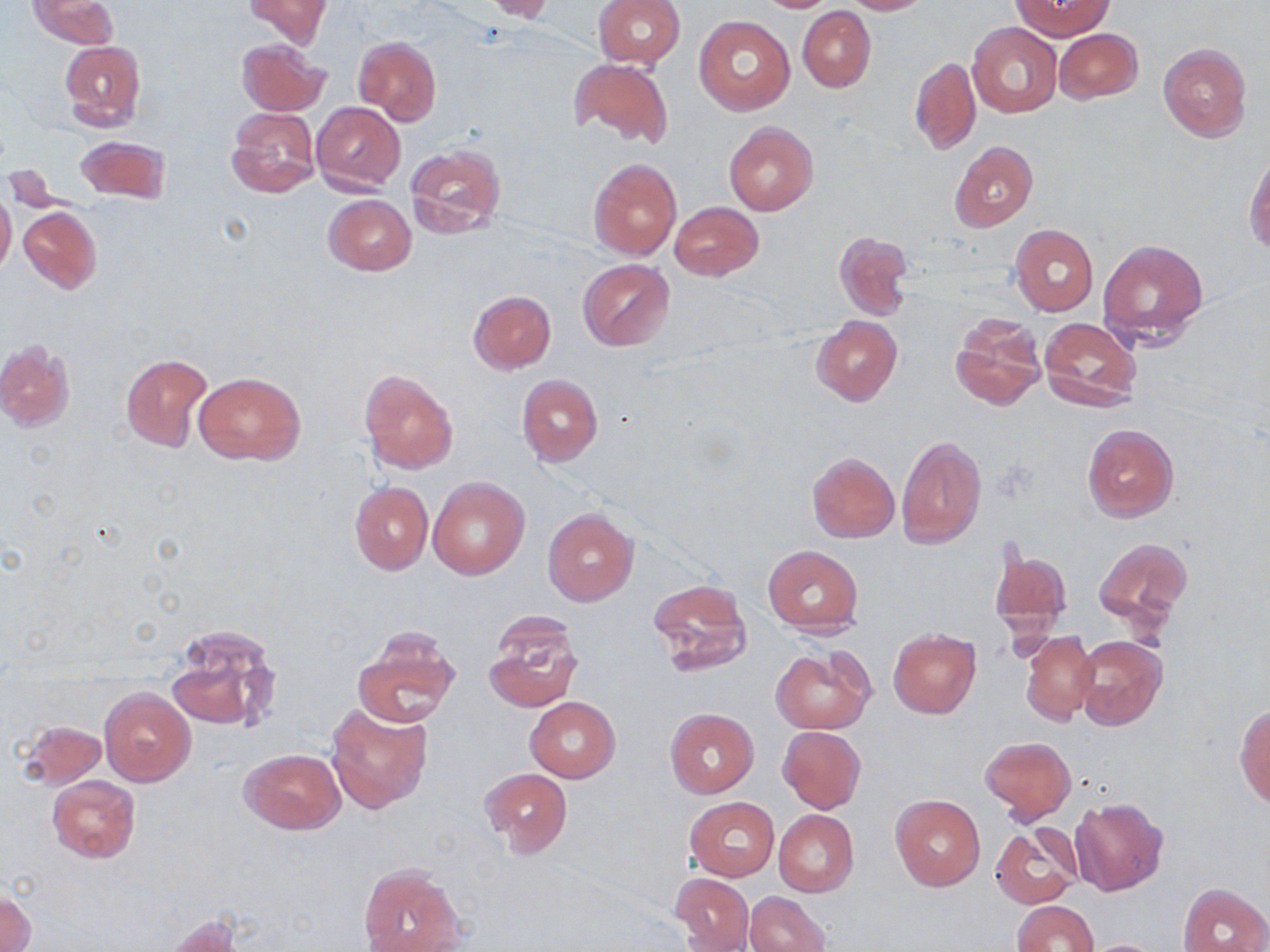

slide-level diagnosis = no evidence of blood parasites
modality = optical microscopy
preparation = thin blood film
image size = 1270×952 pixels
magnification = 1000x
stain = May-Grünwald-Giemsa
field of view = one of a larger specimen
uninfected red blood cell locations = approximate bounding boxes as [x1, y1, x2, y2] in pixels: [27, 0, 119, 50], [243, 0, 330, 49], [483, 0, 558, 23], [594, 0, 684, 69], [753, 0, 839, 13], [841, 0, 932, 14], [1012, 2, 1110, 38], [797, 6, 875, 93], [694, 14, 794, 114], [968, 22, 1061, 118], [1053, 28, 1143, 103], [355, 36, 441, 124], [237, 39, 329, 116], [59, 40, 145, 132], [1157, 43, 1253, 143], [910, 55, 982, 157], [569, 57, 674, 150], [312, 102, 405, 195], [226, 106, 320, 200], [723, 120, 819, 215], [75, 135, 170, 205], [949, 142, 1037, 231], [404, 143, 507, 237], [1245, 149, 1270, 254], [589, 158, 681, 259], [0, 190, 16, 279], [323, 194, 416, 275], [669, 201, 763, 280], [18, 206, 103, 294], [1010, 224, 1097, 316], [832, 230, 915, 322], [1097, 239, 1208, 348], [578, 259, 676, 351], [468, 289, 556, 374], [950, 312, 1046, 412], [812, 316, 902, 405], [1038, 317, 1143, 414], [1, 340, 75, 432], [120, 354, 214, 453], [358, 368, 459, 474], [195, 370, 305, 465], [516, 374, 603, 467], [1082, 424, 1178, 522], [896, 434, 987, 551], [807, 452, 899, 543], [428, 476, 529, 580], [350, 482, 432, 574], [543, 508, 637, 605], [1094, 536, 1193, 633], [763, 545, 863, 635], [988, 545, 1073, 646], [647, 579, 752, 678], [482, 611, 583, 713], [166, 623, 282, 735], [352, 626, 461, 727], [888, 629, 980, 718], [1020, 630, 1098, 725], [1074, 635, 1167, 731], [770, 648, 872, 733], [100, 686, 195, 786], [526, 697, 619, 783], [325, 699, 433, 815], [1236, 702, 1270, 809], [665, 708, 758, 797], [19, 720, 107, 789], [777, 726, 866, 814], [979, 736, 1075, 823], [239, 748, 346, 834], [481, 767, 572, 857], [47, 775, 141, 863], [891, 794, 984, 891], [685, 797, 779, 880], [1069, 797, 1169, 896], [773, 809, 859, 897], [990, 825, 1081, 909], [358, 865, 464, 951], [671, 873, 754, 952], [1180, 884, 1269, 952], [2, 889, 35, 952], [744, 892, 831, 952], [1012, 900, 1097, 951], [165, 914, 242, 952], [1081, 938, 1167, 952]